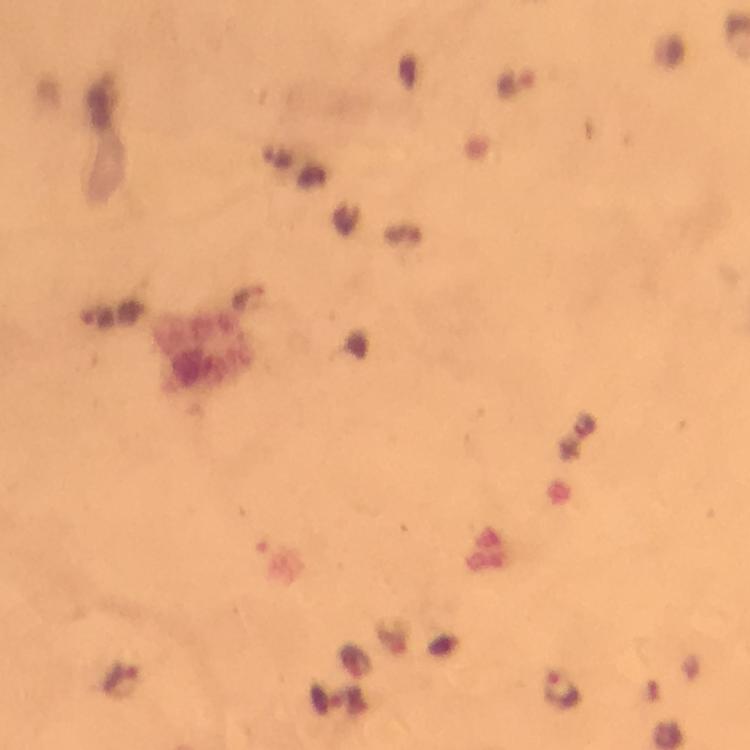
{
  "immersion_oil": "used",
  "magnification": "100x",
  "context": "from a malaria diagnostic workup",
  "cropped_from": "a single field of view",
  "image_size": "750×750 pixels",
  "capture": "smartphone photograph through a microscope",
  "preparation": "thick smear",
  "plasmodium_parasite_locations": "approximate centers as {x, y} in pixels: {516, 84}, {561, 691}",
  "stain": "Giemsa"
}